Locate every blood parasite and identify its species.
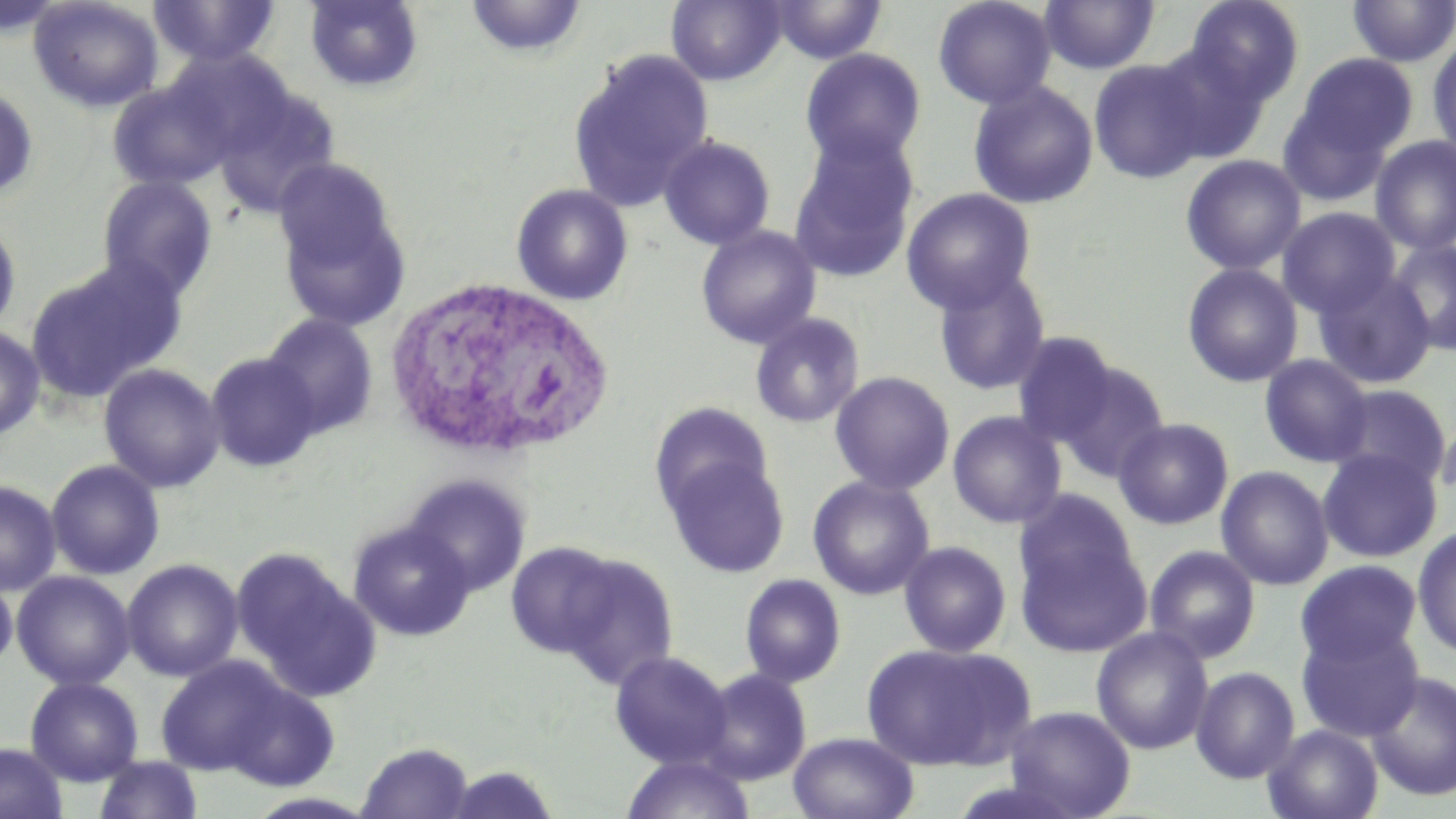

No blood parasites observed.

slide_level_diagnosis: no evidence of blood parasites
modality: light microscopy
stain: May-Grünwald-Giemsa
image_size: 1456×819 pixels
magnification: 1000x
uninfected_red_blood_cell_locations: 'approximate bounding boxes as (x1, y1, x2, y2) in pixels: (28, 0, 164, 112), (148, 0, 282, 69), (465, 0, 589, 60), (666, 0, 786, 86), (933, 0, 1056, 110), (1039, 0, 1160, 75), (1185, 0, 1304, 107), (0, 1, 69, 37), (304, 1, 424, 93), (770, 1, 887, 64), (1346, 1, 1456, 67), (1427, 36, 1456, 162), (1153, 45, 1272, 163), (799, 48, 926, 168), (567, 49, 713, 213), (1294, 53, 1418, 162), (1088, 59, 1212, 184), (107, 78, 236, 191), (968, 81, 1098, 210), (209, 82, 341, 218), (0, 85, 39, 203), (1277, 97, 1394, 206), (788, 131, 920, 284), (658, 135, 775, 250), (1370, 136, 1456, 254), (1180, 155, 1306, 275), (97, 176, 218, 302), (511, 183, 633, 305), (901, 188, 1036, 313), (277, 193, 412, 332), (1278, 207, 1400, 318), (0, 217, 21, 336), (696, 225, 821, 349), (1387, 239, 1455, 355), (26, 258, 182, 403), (1181, 263, 1303, 388), (933, 267, 1052, 396), (1312, 269, 1437, 390), (261, 312, 379, 438), (750, 313, 865, 428), (0, 323, 45, 439), (1011, 332, 1120, 446), (204, 352, 321, 472), (1259, 354, 1373, 467), (1054, 360, 1170, 482), (98, 363, 225, 493), (830, 371, 954, 495), (1328, 383, 1453, 488), (649, 402, 773, 516), (1436, 408, 1455, 512), (948, 411, 1066, 529), (1113, 417, 1234, 530), (1318, 448, 1442, 563), (663, 455, 791, 578), (46, 459, 165, 580), (1215, 465, 1334, 591), (404, 474, 531, 598), (808, 476, 934, 600), (0, 480, 62, 596), (1016, 490, 1140, 604), (347, 521, 475, 642), (1015, 524, 1152, 656), (1412, 527, 1456, 658), (505, 541, 621, 658), (899, 541, 1012, 658), (1144, 545, 1261, 663), (553, 553, 678, 687), (237, 555, 381, 703), (121, 558, 244, 682), (1294, 560, 1423, 670), (12, 570, 135, 690), (740, 573, 846, 688), (0, 574, 17, 674), (1296, 620, 1424, 742), (1091, 627, 1214, 755), (860, 641, 1036, 773), (610, 651, 733, 768), (154, 656, 294, 777), (1190, 666, 1300, 783), (697, 668, 812, 785), (1365, 670, 1456, 801), (25, 677, 144, 786), (216, 677, 341, 791), (1003, 705, 1136, 818), (1263, 725, 1383, 819), (788, 731, 920, 819), (357, 741, 474, 819), (0, 742, 68, 819), (621, 753, 756, 819), (94, 755, 203, 819), (442, 763, 562, 818)'
white_blood_cell_locations: 'approximate bounding boxes as (x1, y1, x2, y2) in pixels: (382, 276, 614, 461)'
field_of_view: one of a larger specimen
preparation: thin blood film